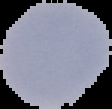

preparation = thin blood smear
malaria status = parasitized
image size = 112×109 pixels
image type = segmented cell region with the area outside set to black